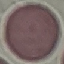
Result: no malaria parasites detected. Automatically extracted cell patch, resized to 64 × 64 pixels. Giemsa-stained preparation. Thin smear of blood. Photographed with a smartphone camera at the microscope eyepiece.